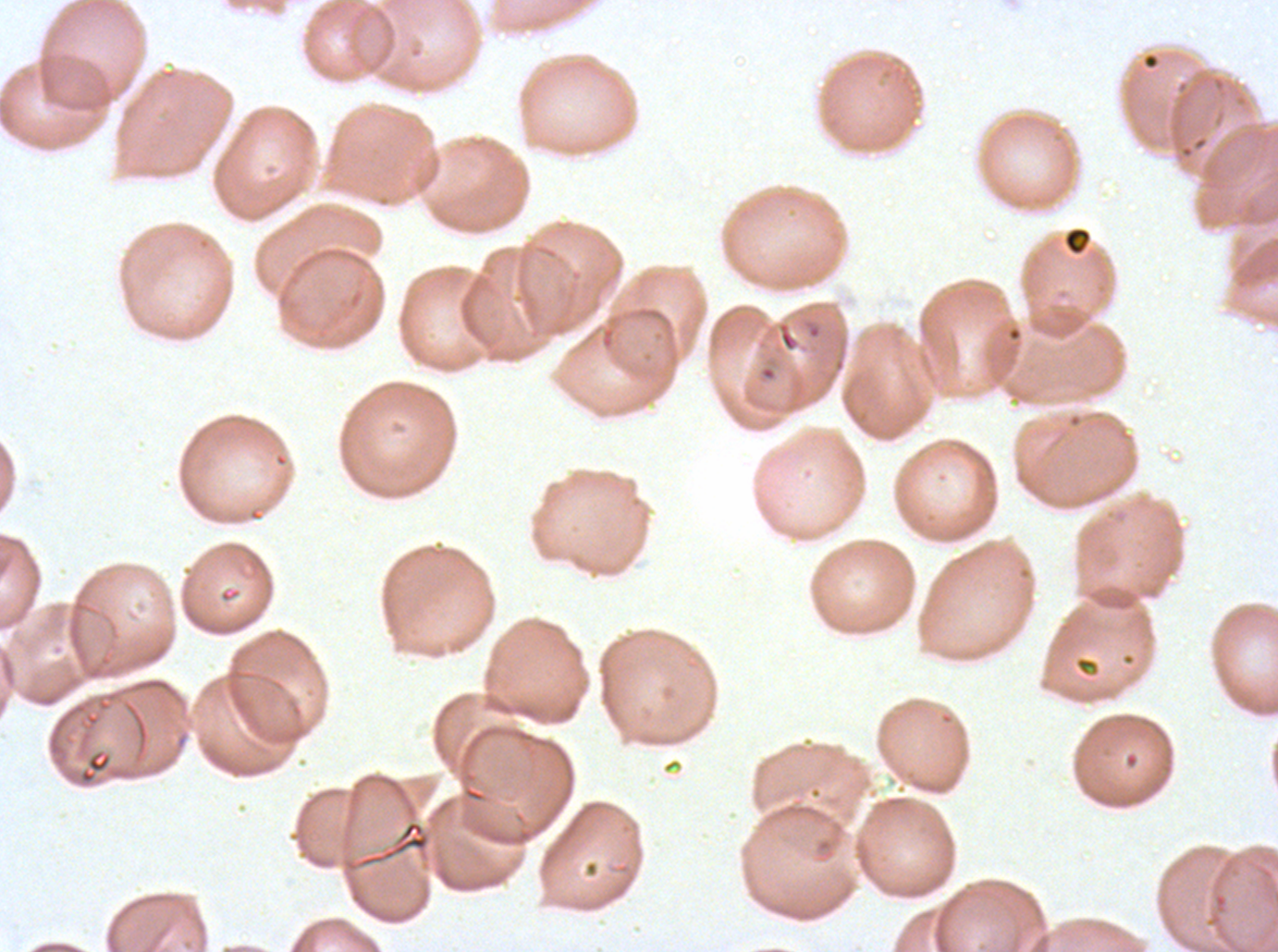
Approximate bounding boxes as [x1, y1, x2, y2] in pixels. Debris locations: [1063, 226, 1092, 255]. Giemsa stain. Plasmodium falciparum cultured ex vivo for 24 to 48 hours, from a patient in The Gambia. Thin blood film. A sub-image separated from a larger composite. Image is 1278×952 pixels.